Classify this cell by malaria status.
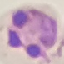

Parasitized.

capture = smartphone through the microscope eyepiece
image type = automatically extracted cell patch, resized to 64 × 64 pixels
preparation = thin smear
stain = Giemsa